Assess the morphology of the red blood cells.
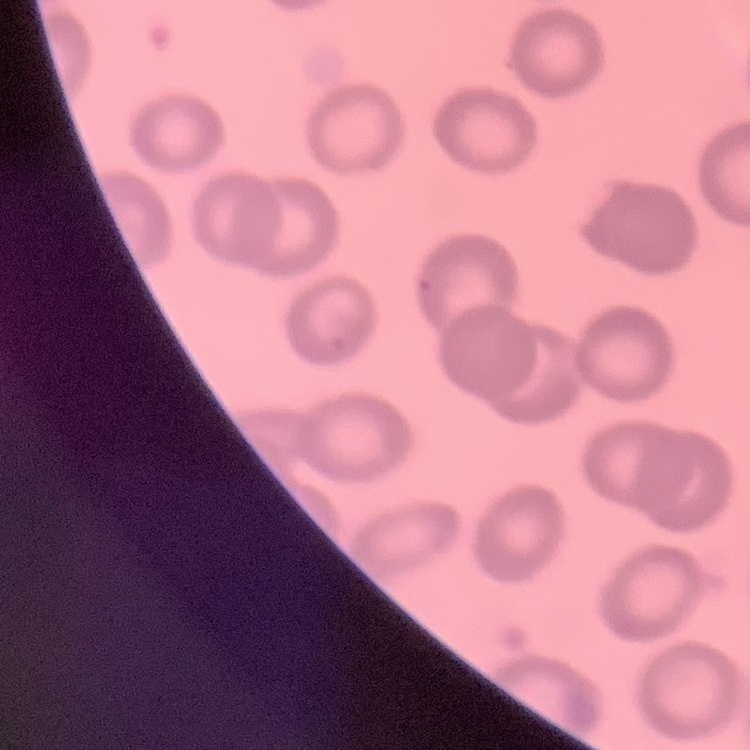
No rouleaux formation.

Thin blood film. Square crop of a larger photomicrograph. Field's or Giemsa stain.